Describe the morphology of the erythrocytes.
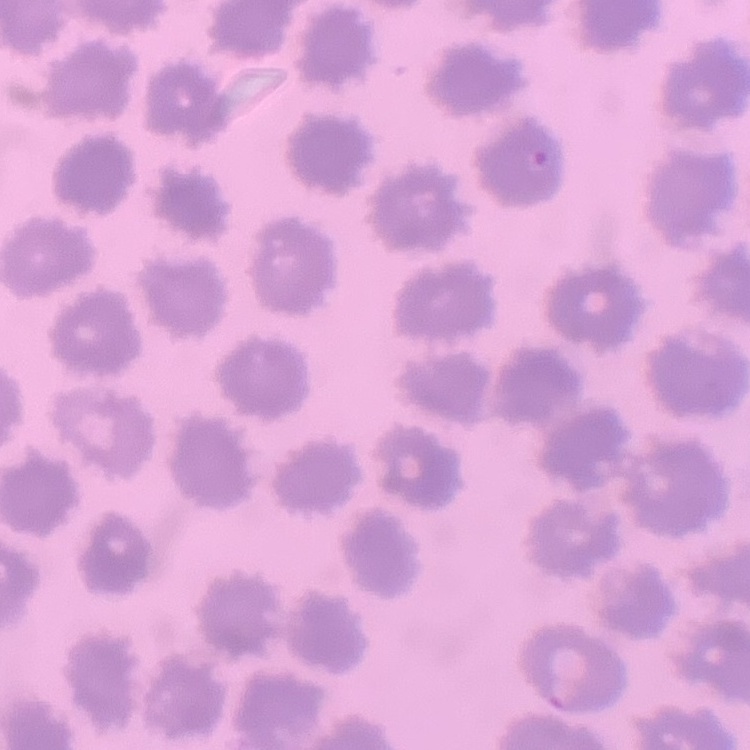

No rouleaux formation.

Thin peripheral smear. One tile cut from a larger photomicrograph. Stained with either Field's or Giemsa.